Assess this cell for malaria.
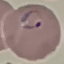
It is parasitized.

Giemsa stain. Photographed with a smartphone camera at the microscope eyepiece. Thin blood film. Automatically extracted cell patch, resized to 64 × 64 pixels.